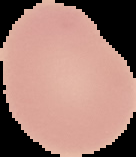
Summary:
  - Preparation: thin blood smear
  - Image type: segmented cell region with the area outside set to black
  - Malaria status: uninfected
  - Image size: 136×157 pixels